Report the malaria status of this cell.
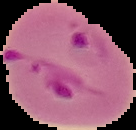

Parasitized.

preparation: thin blood smear
image_size: 136×130 pixels
image_type: segmented cell region with the area outside set to black